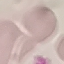
Result: no malaria parasites seen. Giemsa stain. Thin blood smear. Photographed with a smartphone camera at the microscope eyepiece. Cell patch, automatically extracted from a larger field of view and resized to 64 × 64 pixels.